State which parasite is depicted.
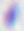
Toxoplasma gondii.

Summary:
  - Modality: photomicrograph
  - Magnification: 400x